Name the parasite shown.
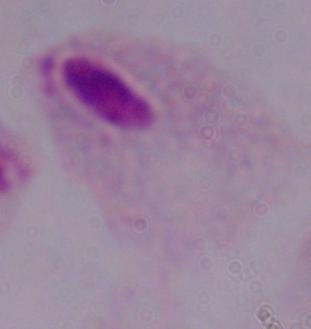

A trichomonad.

Captured at 1000x magnification. Micrograph.